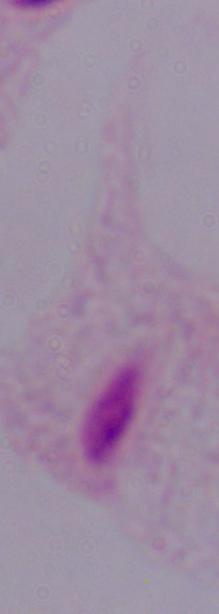
A trichomonad is shown. Micrograph. Captured at 1000x magnification.